State which parasite is depicted.
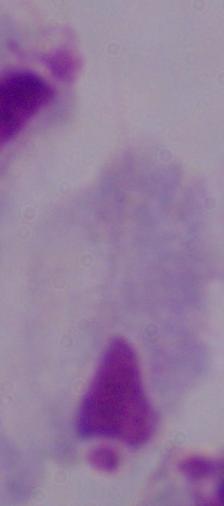
A trichomonad.

modality = micrograph
magnification = 1000x